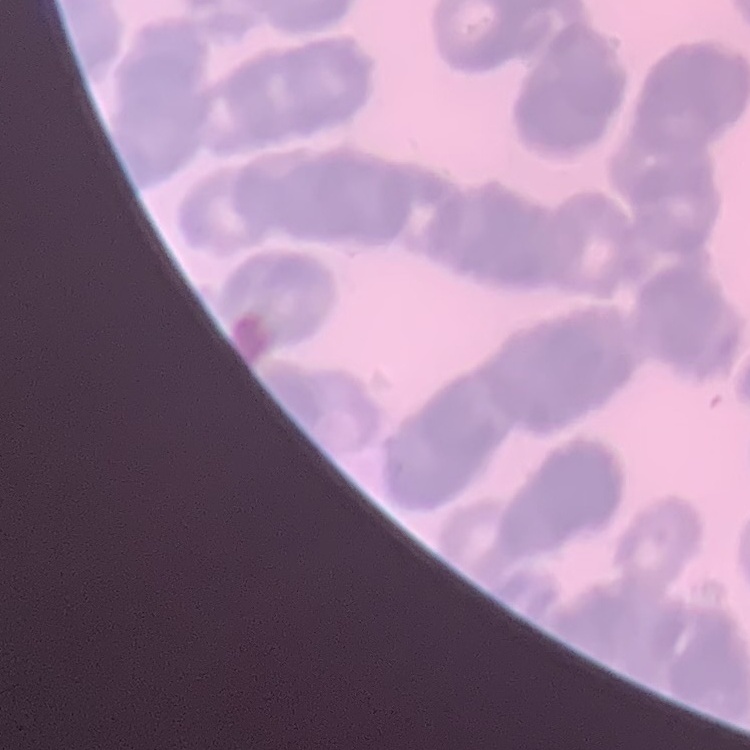

red_blood_cell_morphology: rouleaux formation
stain: Field's or Giemsa
image_type: one tile cut from a larger photomicrograph
preparation: thin blood film